Comment on the morphology of the erythrocytes.
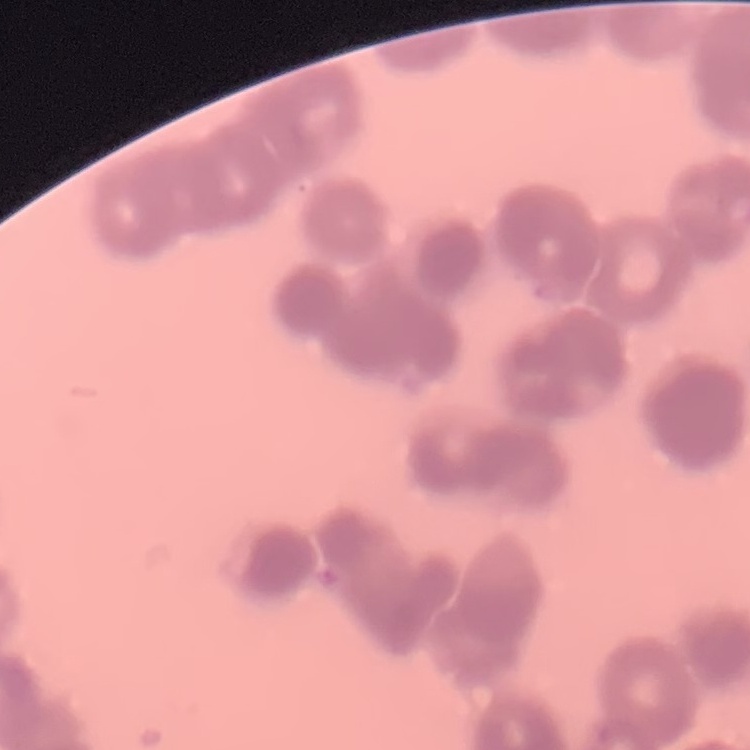

Rouleaux formation.

stain = Field's or Giemsa
preparation = thin blood smear
image type = one tile cut from a larger photomicrograph